Report the malaria status of this cell.
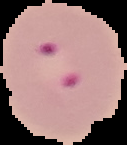
It is parasitized.

{
  "image_type": "cell region segmented out of the field of view; surrounding area masked to black",
  "image_size": "127×145 pixels",
  "preparation": "thin blood film"
}